Report the malaria status of this cell.
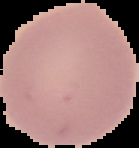
It is uninfected.

preparation = thin blood film
image size = 139×148 pixels
image type = segmented cell region on a black background